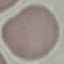 Result: no malaria parasites detected. Thin smear of blood. Automatically extracted cell patch, resized to 64 × 64 pixels. Giemsa-stained preparation. Photographed with a smartphone camera at the microscope eyepiece.